Locate leukocytes (white blood cells).
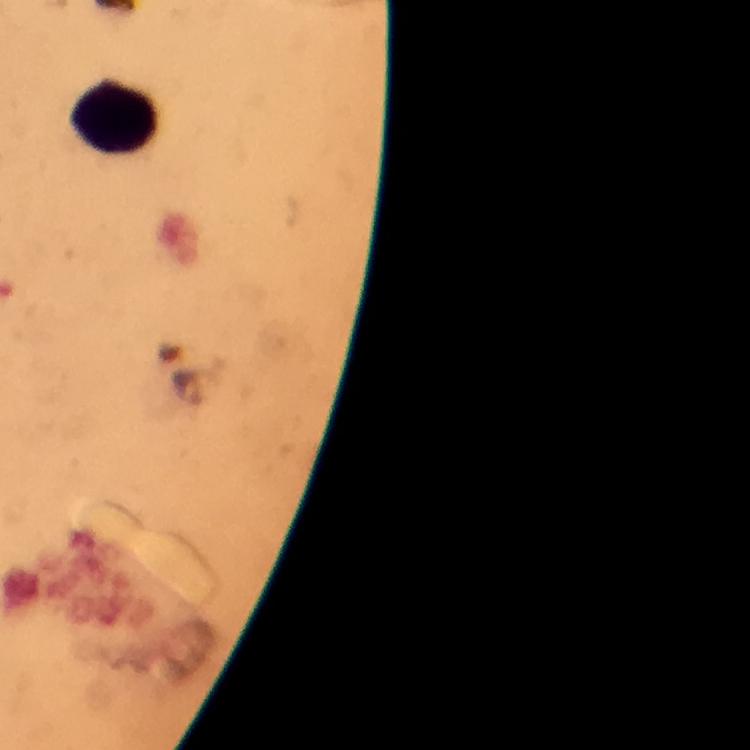
Approximate object centers, in pixels from the top-left corner.
Leukocytes: (x=114, y=119).

Summary:
  - Context: from a diagnostic examination for malaria
  - Image size: 750×750 pixels
  - Cropped from: a single field of view
  - Magnification: 100x
  - Immersion oil: used
  - Preparation: thick blood film
  - Stain: Giemsa
  - Malaria parasites: none seen
  - Capture: smartphone camera through the microscope